Outline each blood parasite and name the species.
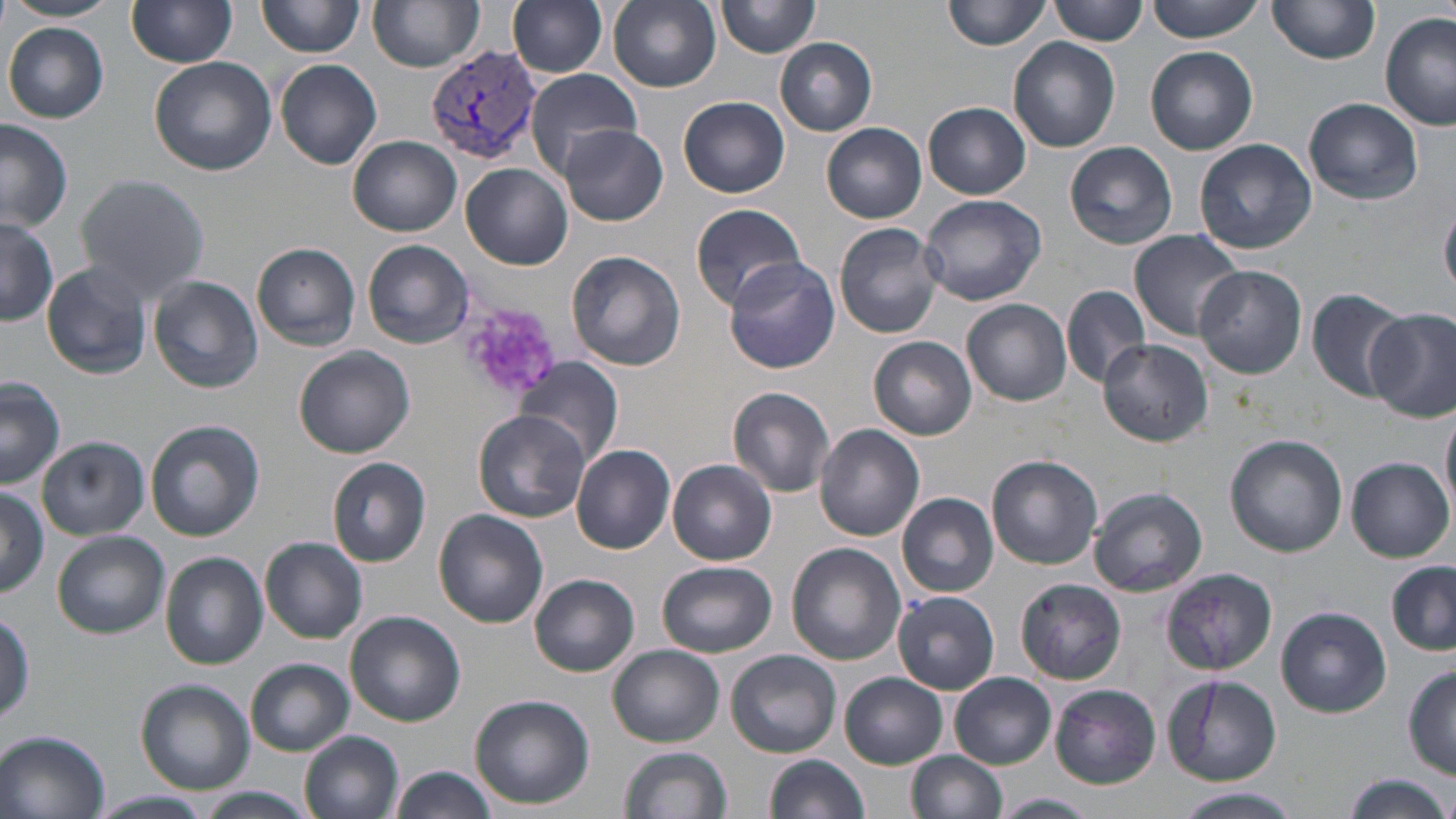
Approximate bounding boxes as [x1, y1, x2, y2] in pixels.
Plasmodium vivax-infected red blood cells: [426, 46, 541, 167].
No Plasmodium falciparum, Plasmodium ovale, Plasmodium malariae, Babesia divergens, or Trypanosoma brucei observed.

slide_level_diagnosis: Plasmodium vivax
stain: May-Grünwald-Giemsa
field_of_view: single
image_size: 1456×819 pixels
preparation: thin blood smear
modality: optical microscopy
platelet_locations: 'approximate bounding boxes as [x1, y1, x2, y2] in pixels: [455, 301, 558, 403]'
magnification: 1000x
uninfected_red_blood_cell_locations: 'approximate bounding boxes as [x1, y1, x2, y2] in pixels: [3, 0, 122, 23], [257, 0, 363, 58], [368, 0, 485, 73], [507, 0, 609, 78], [606, 0, 721, 91], [1049, 0, 1147, 46], [1146, 0, 1267, 41], [127, 1, 236, 70], [717, 1, 821, 59], [942, 1, 1052, 52], [1266, 1, 1378, 68], [1378, 13, 1455, 131], [4, 23, 108, 123], [1009, 37, 1120, 153], [775, 38, 877, 135], [1146, 46, 1258, 155], [150, 57, 277, 177], [274, 60, 383, 169], [524, 69, 641, 173], [679, 95, 791, 198], [1304, 98, 1423, 205], [923, 102, 1030, 198], [0, 120, 73, 232], [822, 123, 928, 223], [561, 125, 668, 227], [349, 135, 462, 236], [1194, 138, 1317, 256], [1064, 141, 1178, 248], [461, 164, 573, 270], [74, 174, 211, 302], [918, 194, 1046, 308], [691, 203, 808, 309], [1441, 204, 1456, 300], [0, 215, 57, 325], [834, 222, 944, 339], [1128, 229, 1245, 342], [362, 239, 475, 349], [251, 243, 361, 350], [565, 249, 686, 371], [724, 257, 840, 374], [41, 262, 153, 379], [1193, 266, 1307, 379], [149, 276, 263, 394], [1062, 285, 1152, 388], [1307, 287, 1410, 400], [962, 297, 1072, 405], [1368, 308, 1456, 421], [869, 335, 977, 439], [1099, 339, 1213, 449], [294, 347, 415, 458], [518, 357, 624, 465], [1, 378, 65, 488], [727, 386, 836, 497], [1442, 405, 1456, 518], [473, 410, 591, 522], [146, 421, 264, 541], [814, 423, 925, 540], [1224, 435, 1349, 556], [39, 437, 148, 540], [571, 443, 677, 554], [986, 453, 1104, 570], [327, 457, 432, 568], [1345, 457, 1453, 562], [668, 459, 776, 565], [0, 486, 46, 598], [1089, 486, 1207, 597], [897, 492, 999, 598], [435, 509, 548, 628], [53, 530, 169, 638], [261, 537, 369, 644], [786, 543, 905, 665], [160, 552, 268, 668], [657, 562, 777, 657], [1386, 563, 1456, 655], [1161, 569, 1277, 675], [529, 574, 640, 677], [1016, 579, 1126, 685], [893, 589, 1000, 694], [1276, 606, 1390, 718], [346, 611, 465, 726], [0, 612, 33, 730], [607, 645, 724, 747], [726, 650, 843, 757], [245, 658, 356, 758], [1402, 668, 1456, 778], [950, 673, 1055, 768], [840, 674, 948, 768], [1160, 674, 1283, 786], [137, 679, 255, 794], [1050, 685, 1161, 788], [470, 693, 595, 809], [0, 731, 109, 818], [300, 731, 404, 819], [621, 745, 732, 819], [906, 750, 1007, 819], [763, 754, 871, 819], [390, 765, 501, 819], [1340, 774, 1452, 819], [197, 786, 315, 819], [1170, 789, 1304, 819], [92, 790, 215, 819], [992, 793, 1099, 819]'